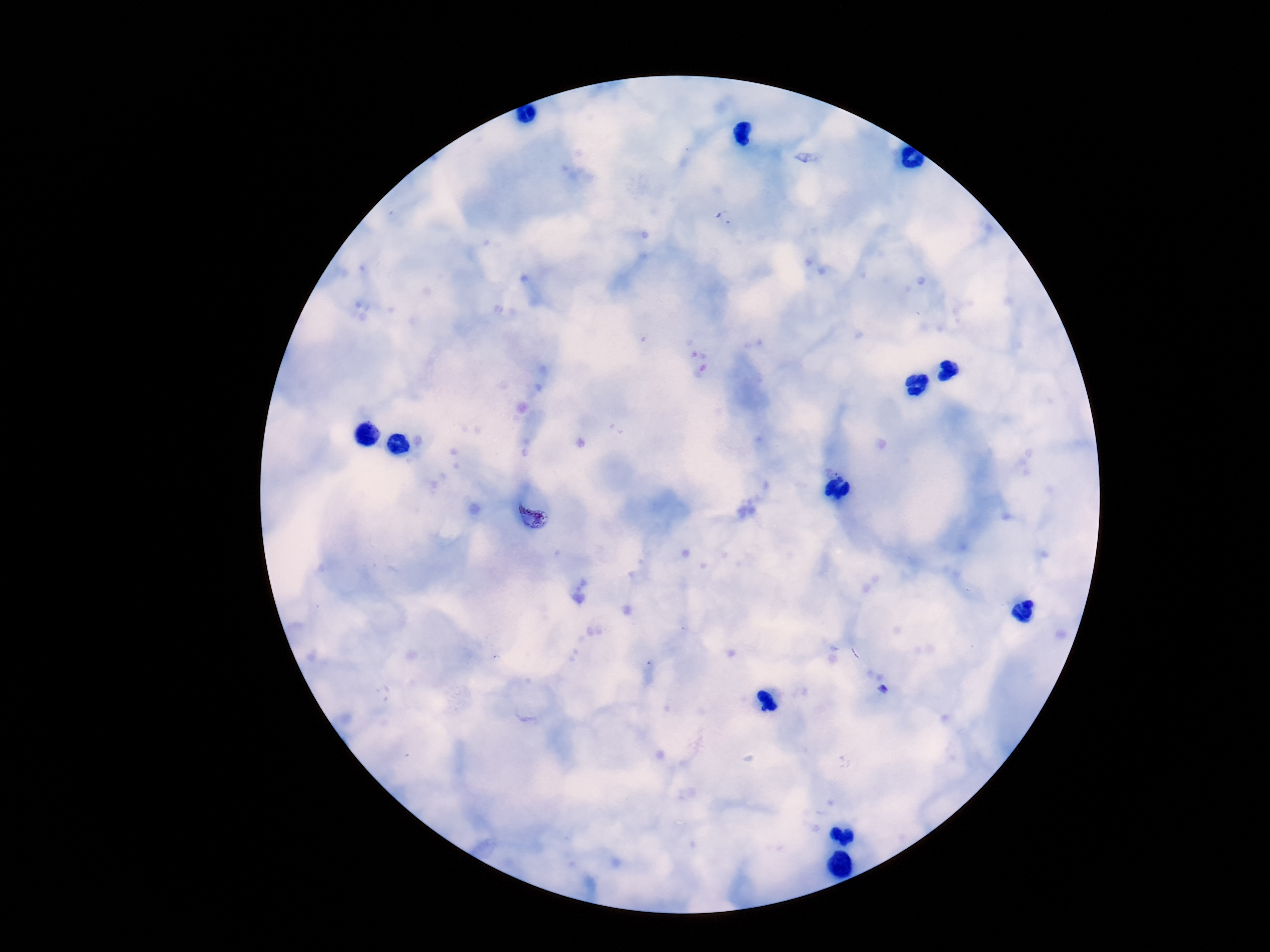
Approximate object centers, in pixels from the top-left corner.
Summary:
  - Plasmodium parasite locations: (x=532, y=516), (x=882, y=689)
  - Magnification: 100x
  - Capture: smartphone camera through the microscope eyepiece
  - Image size: 1270×952 pixels
  - Patient malaria status: positive
  - Field of view: one from this slide
  - Preparation: thick peripheral-blood smear
  - Stain: Giemsa